Outline each Trypanosoma brucei.
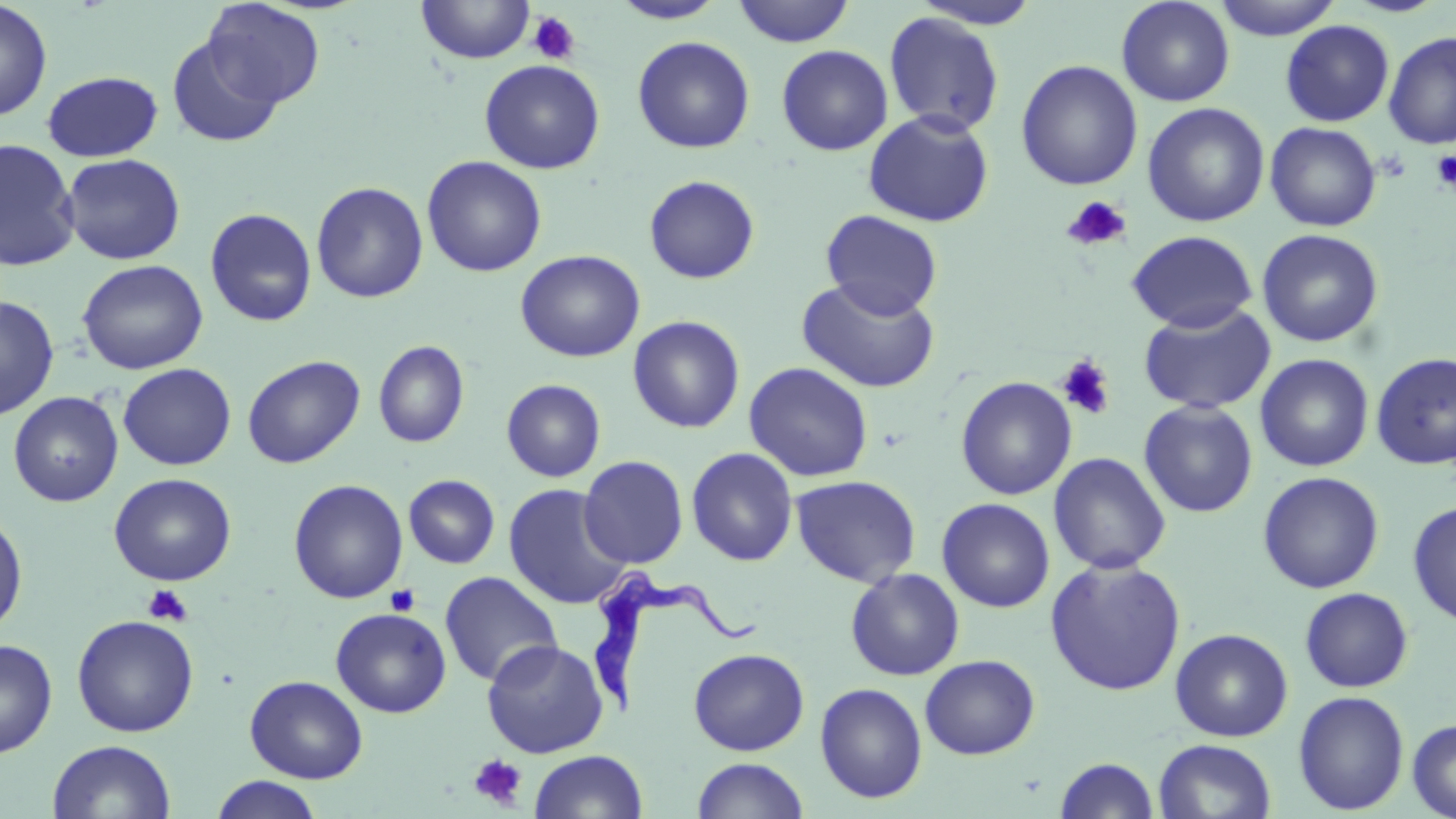

Approximate bounding boxes as (x1,y1)-(x2,y2) corner pairs in pixels.
Trypanosoma brucei: (579,567)-(759,717).

Uninfected red blood cell locations: (416,0)-(536,65), (732,0)-(856,47), (1116,0)-(1235,106), (1213,0)-(1343,40), (1341,0)-(1452,18), (0,1)-(53,121), (202,1)-(326,108), (609,1)-(727,24), (911,1)-(1044,29), (883,12)-(1005,136), (1280,20)-(1394,127), (1382,31)-(1456,150), (166,35)-(285,148), (632,36)-(755,153), (776,45)-(893,156), (479,59)-(605,174), (1015,59)-(1143,191), (41,70)-(163,162), (1142,102)-(1270,227), (863,109)-(994,228), (1264,122)-(1382,232), (0,139)-(80,272), (61,153)-(185,265), (422,155)-(547,277), (644,175)-(760,284), (311,181)-(429,304), (204,208)-(317,327), (820,209)-(943,319), (1256,228)-(1384,347), (1126,230)-(1258,332), (515,249)-(645,362), (77,259)-(208,375), (796,276)-(941,393), (1,295)-(59,420), (1138,302)-(1276,414), (627,315)-(745,433), (373,339)-(470,448), (1371,352)-(1456,469), (242,354)-(365,469), (1255,354)-(1374,472), (744,361)-(873,482), (118,363)-(236,470), (955,376)-(1077,500), (501,379)-(606,482), (8,391)-(123,507), (1139,401)-(1258,517), (686,447)-(798,567), (1048,452)-(1171,575), (578,455)-(689,569), (1257,471)-(1385,593), (109,473)-(236,585), (791,474)-(921,587), (403,475)-(500,569), (288,479)-(409,604), (503,484)-(631,610), (937,498)-(1055,613), (1408,501)-(1456,628), (0,508)-(28,637), (1045,557)-(1186,696), (845,568)-(965,681), (439,571)-(563,688), (1299,587)-(1413,692), (330,607)-(451,718), (72,614)-(199,737), (1170,628)-(1293,741), (0,639)-(57,758), (481,639)-(608,758), (688,648)-(810,755), (920,654)-(1040,759), (245,675)-(368,783), (815,682)-(927,803), (1293,690)-(1410,815), (1407,717)-(1456,818), (1153,738)-(1276,819), (47,739)-(176,819), (529,750)-(648,818), (691,757)-(810,818), (1055,757)-(1160,818), (210,775)-(325,819). Platelet locations: (527,11)-(580,65), (1431,150)-(1456,191), (1062,196)-(1131,252), (1055,355)-(1116,420), (142,584)-(192,626), (385,584)-(420,616), (468,753)-(528,811). Slide-level diagnosis: Trypanosoma brucei. May-Grünwald-Giemsa stain. Thin blood film. One field of a larger specimen. 1000x magnification. Image is 1456×819 pixels. Optical microscopy.